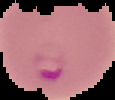 Image is 115×100 pixels. Segmented cell region on a black background. Result: malaria parasites detected. From a thin blood film.